Locate every Plasmodium parasite.
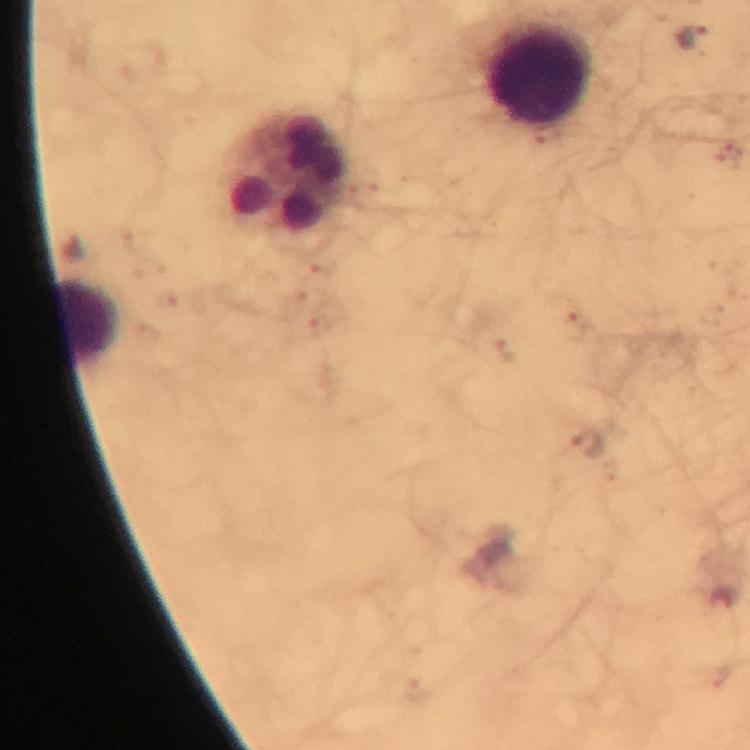
Approximate object centers, in pixels from the top-left corner.
Plasmodium parasites: (x=693, y=39), (x=548, y=134), (x=727, y=155), (x=321, y=266), (x=168, y=302), (x=294, y=302), (x=319, y=326), (x=574, y=327), (x=504, y=350), (x=585, y=441), (x=723, y=600).

cropped from = one field of view
preparation = thick blood smear
capture = smartphone photograph through a microscope
image size = 750×750 pixels
immersion oil = applied
leukocyte locations = approximate object centers, in pixels from the top-left corner: (x=539, y=72), (x=285, y=172), (x=87, y=321)
stain = Giemsa
context = from a diagnostic examination for malaria
magnification = 100x